Report the malaria status of this cell.
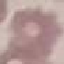

Uninfected.

stain = Giemsa
image type = cell patch, automatically extracted from a larger field of view and resized to 64 × 64 pixels
capture = smartphone through the microscope eyepiece
preparation = thin smear